Locate every blood parasite and identify its species.
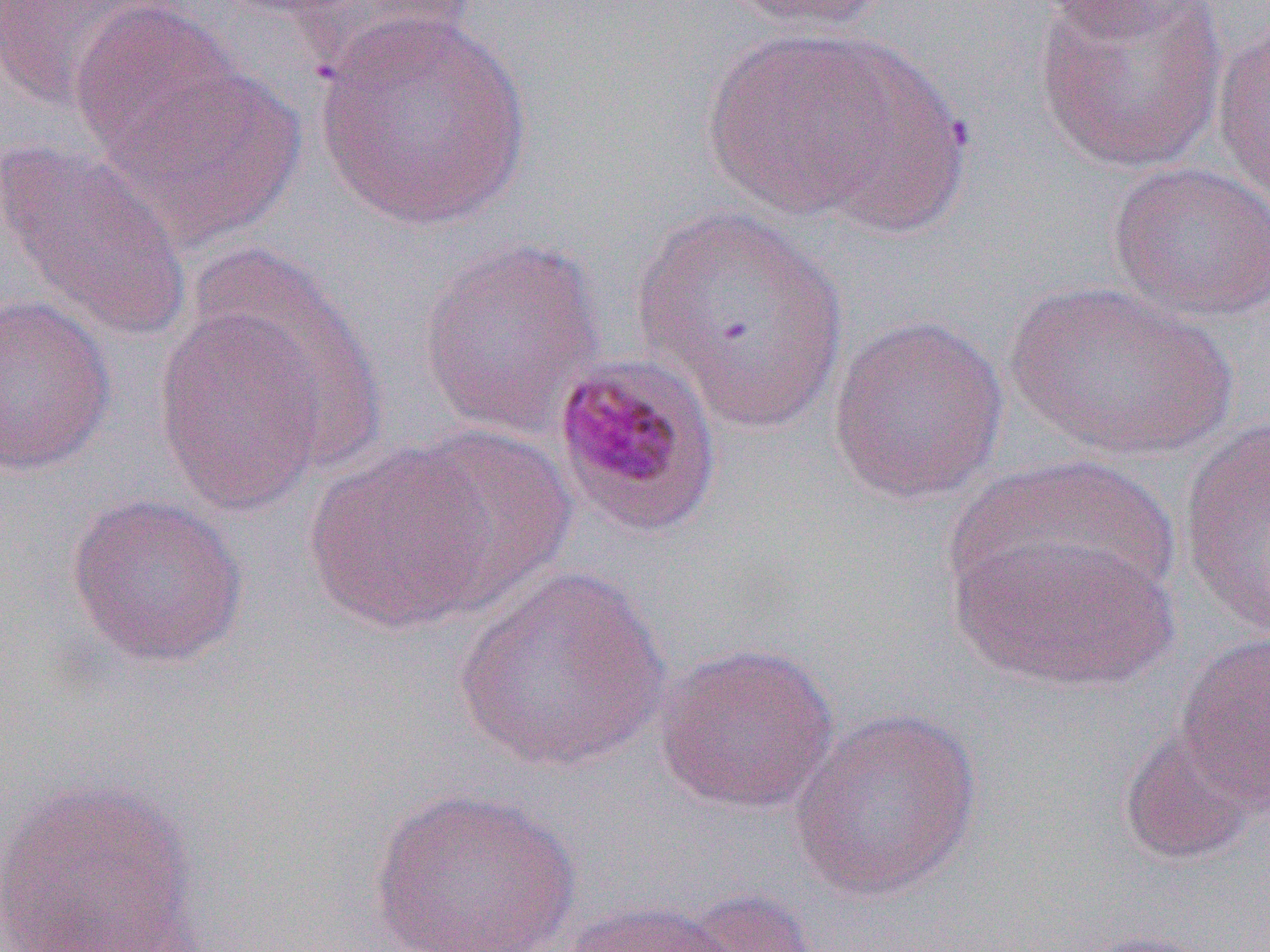

Approximate bounding boxes as [x1, y1, x2, y2] in pixels.
Plasmodium malariae-infected red blood cells: [550, 351, 723, 539].
No Plasmodium falciparum, Plasmodium ovale, Plasmodium vivax, Babesia divergens, or Trypanosoma brucei observed.

Summary:
  - Uninfected red blood cell locations: [0, 0, 184, 112], [287, 0, 483, 84], [720, 0, 894, 34], [1030, 0, 1222, 44], [1031, 1, 1230, 175], [69, 3, 243, 165], [313, 11, 534, 232], [1210, 16, 1269, 214], [689, 25, 949, 229], [102, 63, 305, 250], [0, 139, 194, 344], [1107, 161, 1270, 323], [630, 206, 848, 431], [417, 234, 609, 440], [187, 239, 389, 473], [1004, 279, 1240, 462], [0, 294, 117, 476], [154, 302, 332, 517], [827, 313, 1009, 504], [1177, 417, 1270, 639], [401, 424, 578, 613], [304, 441, 498, 634], [947, 458, 1183, 627], [64, 493, 249, 668], [947, 526, 1179, 694], [452, 566, 674, 776], [1175, 632, 1270, 809], [653, 642, 840, 814], [788, 705, 983, 902], [1117, 723, 1267, 867], [1, 775, 205, 952], [367, 786, 581, 952], [678, 887, 821, 952], [558, 899, 744, 952], [1068, 928, 1224, 952]
  - Slide-level diagnosis: Plasmodium malariae
  - Preparation: thin blood smear
  - Image size: 1270×952 pixels
  - Field of view: single
  - Magnification: 1000x
  - Modality: optical microscopy